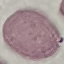
Summary:
  - Malaria status: uninfected
  - Stain: Giemsa
  - Image type: automatically extracted cell patch, resized to 64 × 64 pixels
  - Preparation: thin smear
  - Capture: smartphone camera at the microscope eyepiece